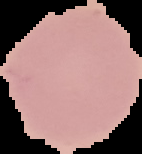
{
  "image_size": "142×154 pixels",
  "preparation": "thin blood smear",
  "malaria_status": "uninfected",
  "image_type": "segmented cell region with the area outside set to black"
}